Comment on the morphology of the erythrocytes.
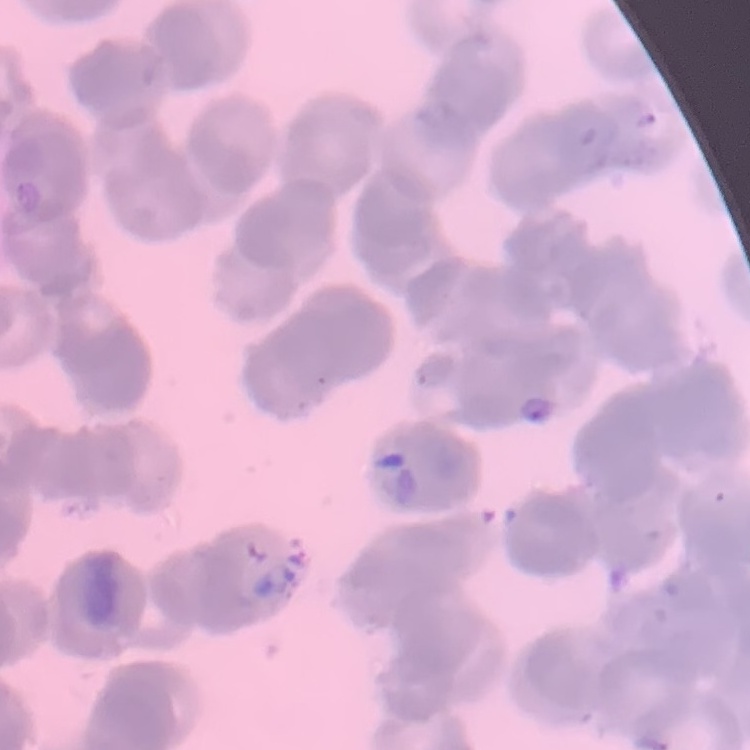

Rouleaux formation.

stain = Field's or Giemsa
preparation = thin blood film
image type = one tile cut from a larger photomicrograph